Locate Plasmodium parasites and leukocytes.
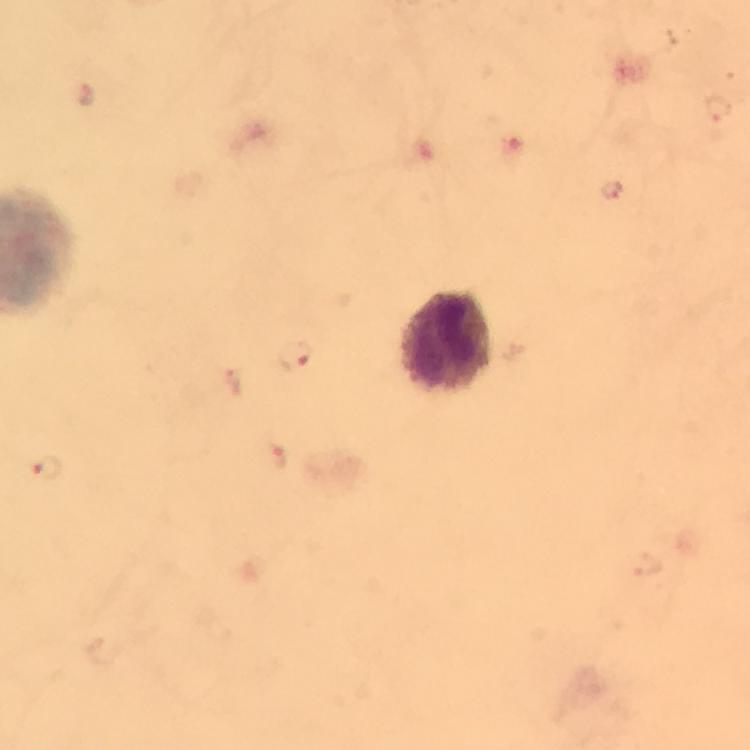
Approximate centers as {x, y} in pixels.
Plasmodium parasites: {717, 109}, {611, 190}, {294, 355}, {277, 458}, {47, 469}.
Leukocytes: {448, 340}.

Giemsa stain. Thick blood film. From a diagnostic examination for malaria. Image is 750×750 pixels. Immersion oil was used. Cropped region of a single field of view. 100x magnification. Photographed through the microscope with a smartphone camera.